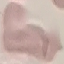
Malaria status: uninfected. Thin blood film. Giemsa stain. Automatically extracted cell patch, resized to 64 × 64 pixels. Photographed with a smartphone camera at the microscope eyepiece.